Name the parasite shown.
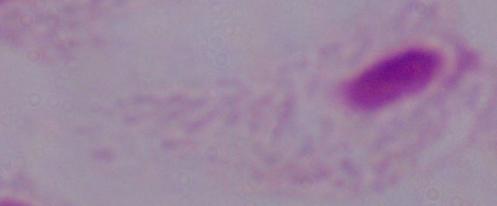
This is a trichomonad.

{
  "magnification": "1000x",
  "modality": "photomicrograph"
}